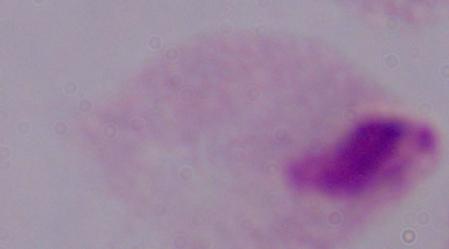
Summary:
  - Magnification: 1000x
  - Identification: trichomonad
  - Modality: photomicrograph